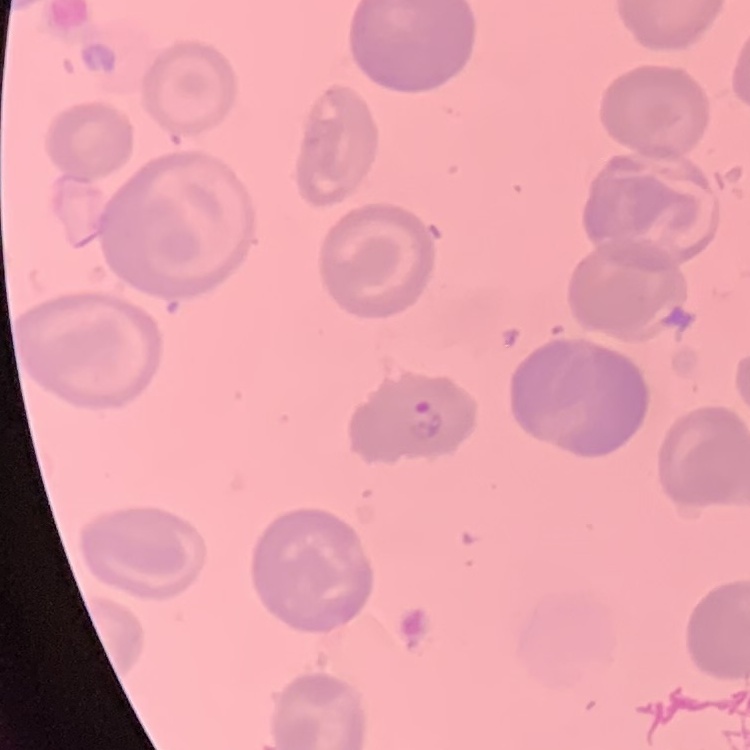 The red blood cells exhibit no rouleaux formation. Square crop of a larger photomicrograph. Stained with either Field's or Giemsa. Thin blood film.